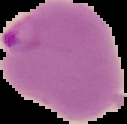

Summary:
  - Image size: 127×124 pixels
  - Preparation: thin blood smear
  - Image type: segmented cell region with the area outside set to black
  - Result: Plasmodium parasites detected